Classify this cell by malaria status.
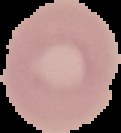

Uninfected.

{
  "image_size": "121×133 pixels",
  "image_type": "segmented cell region with the area outside set to black",
  "preparation": "thin blood film"
}